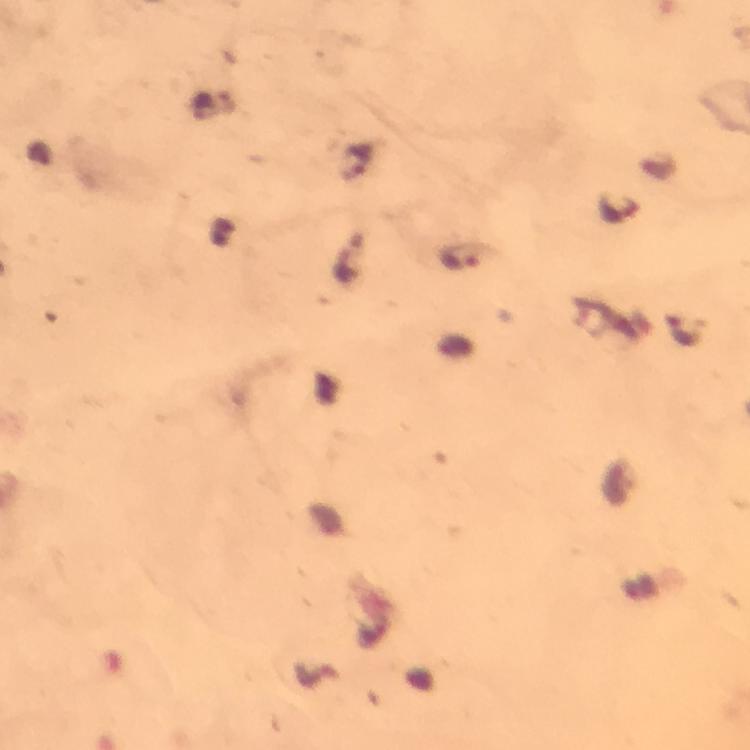
Approximate centers as (x, y) in pixels.
Summary:
  - Plasmodium parasite locations: (357, 159), (618, 210), (464, 259), (683, 330)
  - Preparation: thick blood film
  - Cropped from: one field of view
  - Capture: smartphone mounted on the microscope
  - Stain: Giemsa
  - Image size: 750×750 pixels
  - Immersion oil: used
  - Magnification: 100x
  - Context: from a diagnostic examination for malaria